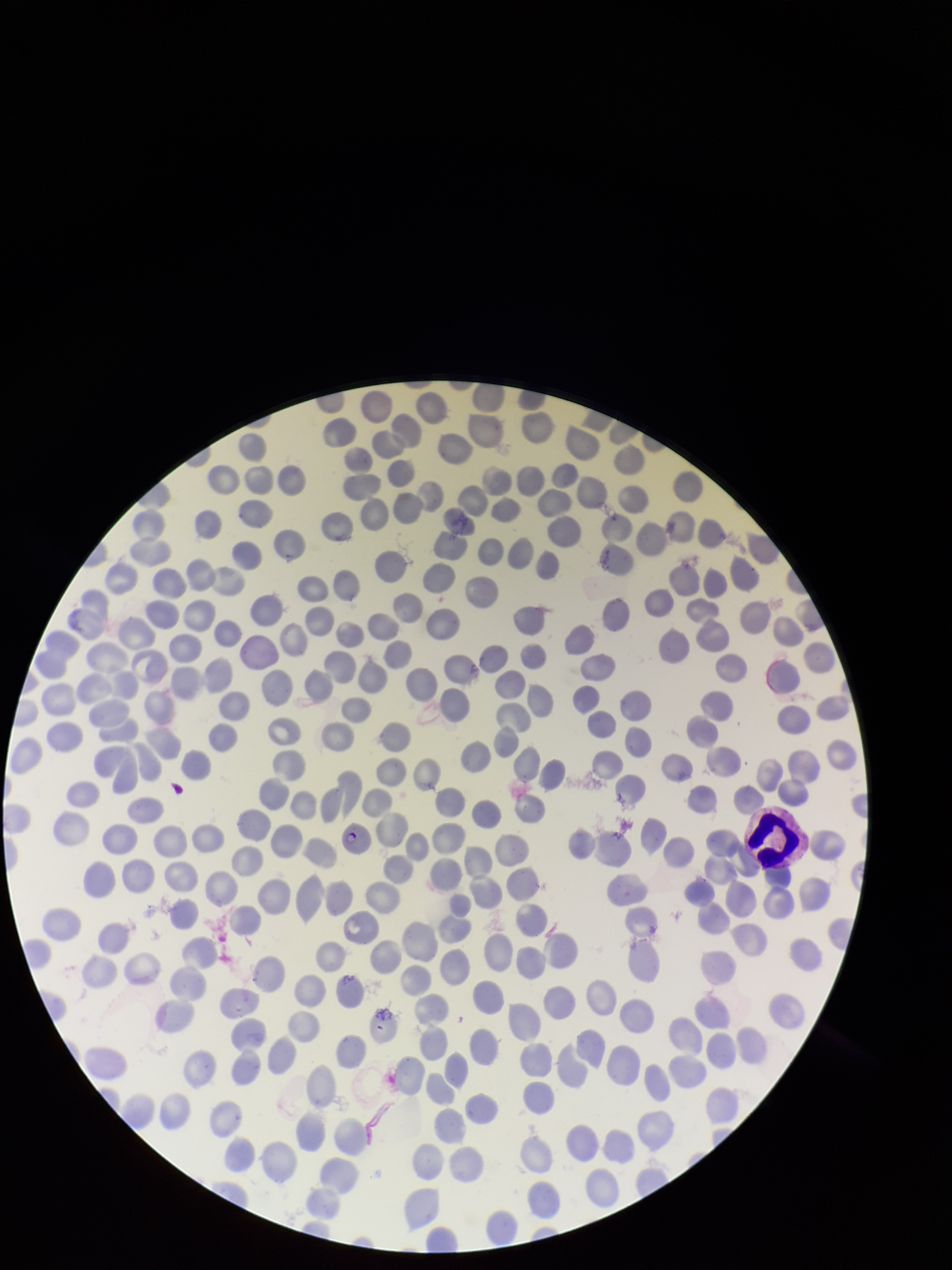

Giemsa stain. Smartphone photograph taken through the eyepiece of a microscope. Species reported for this patient: Plasmodium falciparum. Red blood cell count: 270. One field from this slide. Patient malaria status: positive. Parasitized red blood cells: detected. Preparation: thin. Image is 952×1270 pixels. Parasitized red blood cell count: 1.